Identify the parasite.
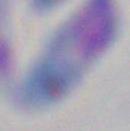

Toxoplasma gondii.

modality = micrograph
magnification = 1000x